Locate every Plasmodium falciparum parasite and give its life-cycle stage, and locate every leukocyte and any debris.
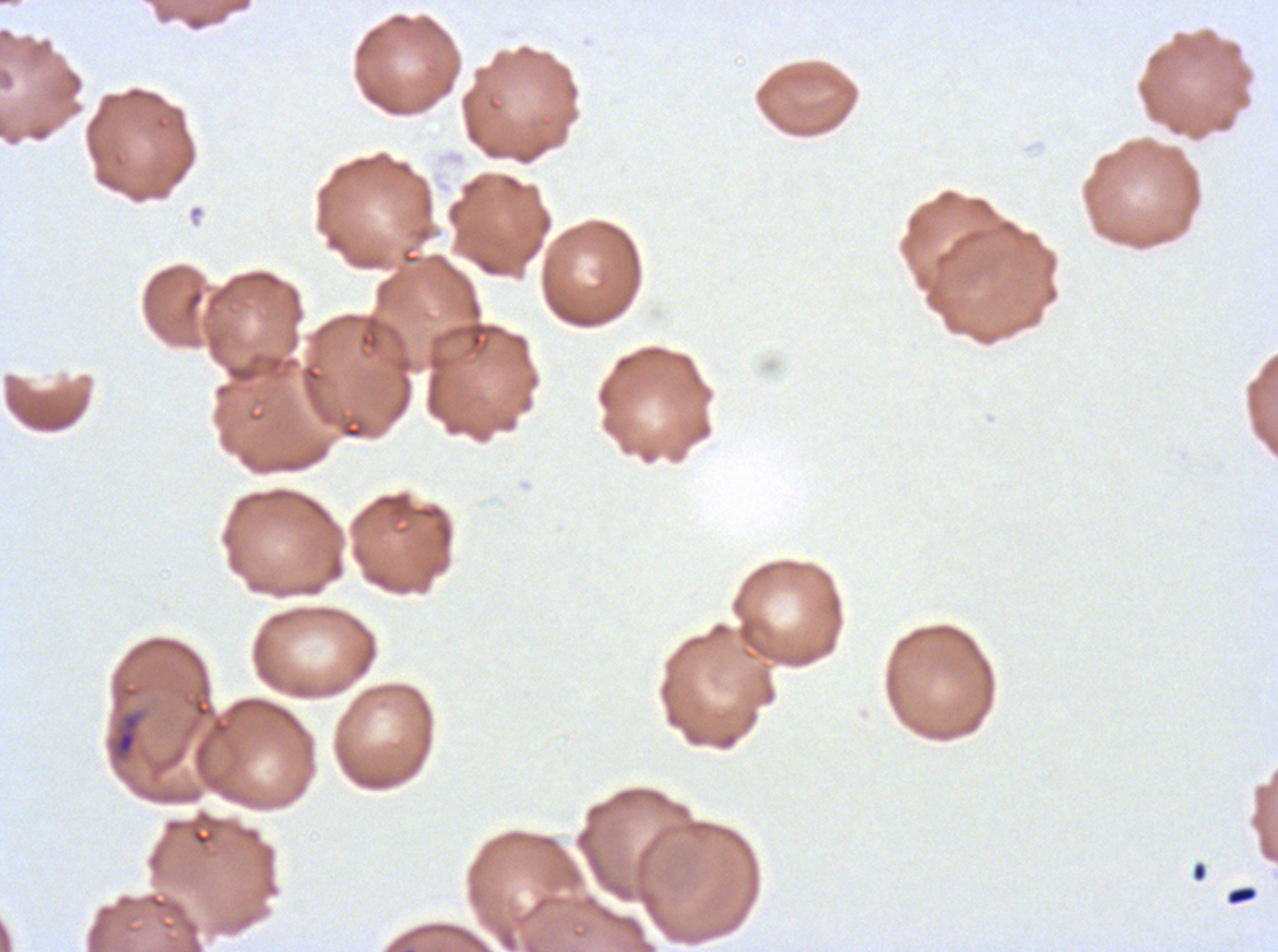

Approximate bounding boxes as (x1, y1, x2, y2) in pixels.
Debris: (113, 712, 141, 760), (1225, 885, 1258, 906).
No rings, late-ring/early-trophozoite forms, mid trophozoites, late trophozoites, early schizonts, late schizonts, segmenters, gametocytes, or leukocytes observed.

One sub-image of a larger composite. Plasmodium falciparum from a patient in The Gambia, cultured ex vivo for 24 to 48 hours. Giemsa stain. Thin blood film. Image is 1278×952 pixels.